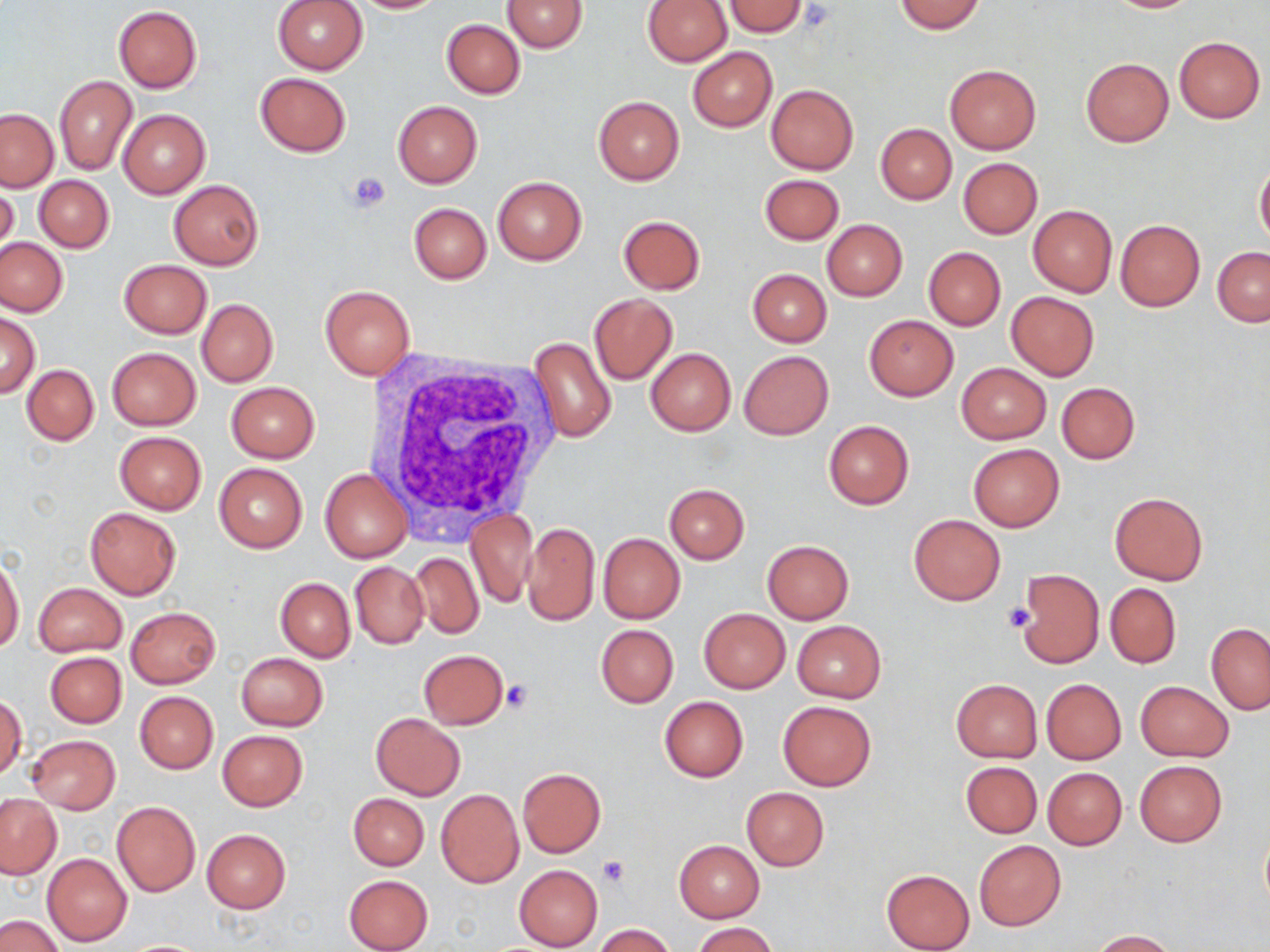

slide-level diagnosis = negative for blood parasites
uninfected red blood cell locations = approximate bounding boxes as (x1,y1)-(x2,y2) corner pairs in pixels: (273,0)-(367,74), (348,0)-(451,14), (501,0)-(588,51), (723,0)-(809,37), (1103,0)-(1201,13), (642,1)-(732,66), (892,1)-(986,34), (114,6)-(202,92), (441,19)-(525,98), (1174,36)-(1265,123), (687,47)-(777,132), (1081,57)-(1173,146), (943,65)-(1041,155), (255,72)-(350,156), (54,74)-(137,175), (766,84)-(858,174), (593,96)-(684,185), (393,100)-(483,188), (0,108)-(59,192), (118,109)-(210,199), (876,123)-(956,204), (957,157)-(1043,238), (1254,161)-(1270,249), (759,174)-(844,246), (34,176)-(114,252), (492,177)-(586,264), (168,179)-(265,271), (1,182)-(19,266), (408,202)-(490,283), (1028,205)-(1117,297), (618,215)-(706,294), (821,219)-(907,301), (1115,219)-(1205,311), (0,237)-(67,316), (924,247)-(1005,330), (1212,247)-(1270,325), (119,259)-(212,339), (748,269)-(831,347), (320,285)-(415,380), (1006,292)-(1099,380), (588,293)-(676,385), (196,299)-(277,387), (1,312)-(40,397), (863,315)-(958,400), (527,336)-(617,444), (107,347)-(201,429), (645,347)-(735,435), (738,351)-(834,439), (956,362)-(1051,444), (22,365)-(99,444), (226,382)-(319,462), (1056,382)-(1140,463), (823,419)-(914,509), (114,431)-(206,515), (969,443)-(1063,531), (213,463)-(307,554), (321,467)-(412,563), (664,483)-(749,564), (1109,492)-(1208,585), (83,507)-(181,600), (466,509)-(537,608), (908,514)-(1005,605), (522,521)-(599,626), (598,533)-(685,623), (762,541)-(853,624), (408,552)-(483,640), (0,556)-(24,652), (350,561)-(429,649), (1017,568)-(1104,668), (275,577)-(355,662), (33,582)-(127,657), (1105,583)-(1181,669), (126,607)-(221,688), (699,608)-(790,693), (792,621)-(885,703), (1206,623)-(1270,715), (596,624)-(678,707), (418,649)-(509,730), (43,651)-(127,728), (234,652)-(329,731), (950,679)-(1042,763), (1041,679)-(1126,763), (1134,680)-(1234,762), (134,691)-(218,772), (1,695)-(25,781), (658,696)-(748,781), (778,700)-(875,790), (370,713)-(465,800), (217,730)-(308,810), (26,735)-(120,813), (1134,759)-(1227,848), (960,760)-(1042,838), (517,767)-(603,857), (1043,767)-(1127,850), (740,786)-(828,872), (436,789)-(524,888), (348,792)-(429,870), (1,794)-(62,879), (111,801)-(201,897), (201,829)-(291,914), (974,839)-(1066,930), (674,840)-(765,922), (42,853)-(133,946), (514,865)-(603,950), (881,868)-(975,952), (343,873)-(434,952), (0,914)-(65,952), (692,923)-(777,952), (594,924)-(676,952), (1090,929)-(1175,951), (119,939)-(213,951)
image size = 1270×952 pixels
white blood cell locations = approximate bounding boxes as (x1,y1)-(x2,y2) corner pairs in pixels: (370,352)-(565,537)
platelet locations = approximate bounding boxes as (x1,y1)-(x2,y2) corner pairs in pixels: (348,170)-(390,210), (1004,603)-(1034,633), (501,679)-(534,713), (599,856)-(629,887)
field of view = single
modality = light microscopy
stain = May-Grünwald-Giemsa
preparation = thin blood film
magnification = 1000x